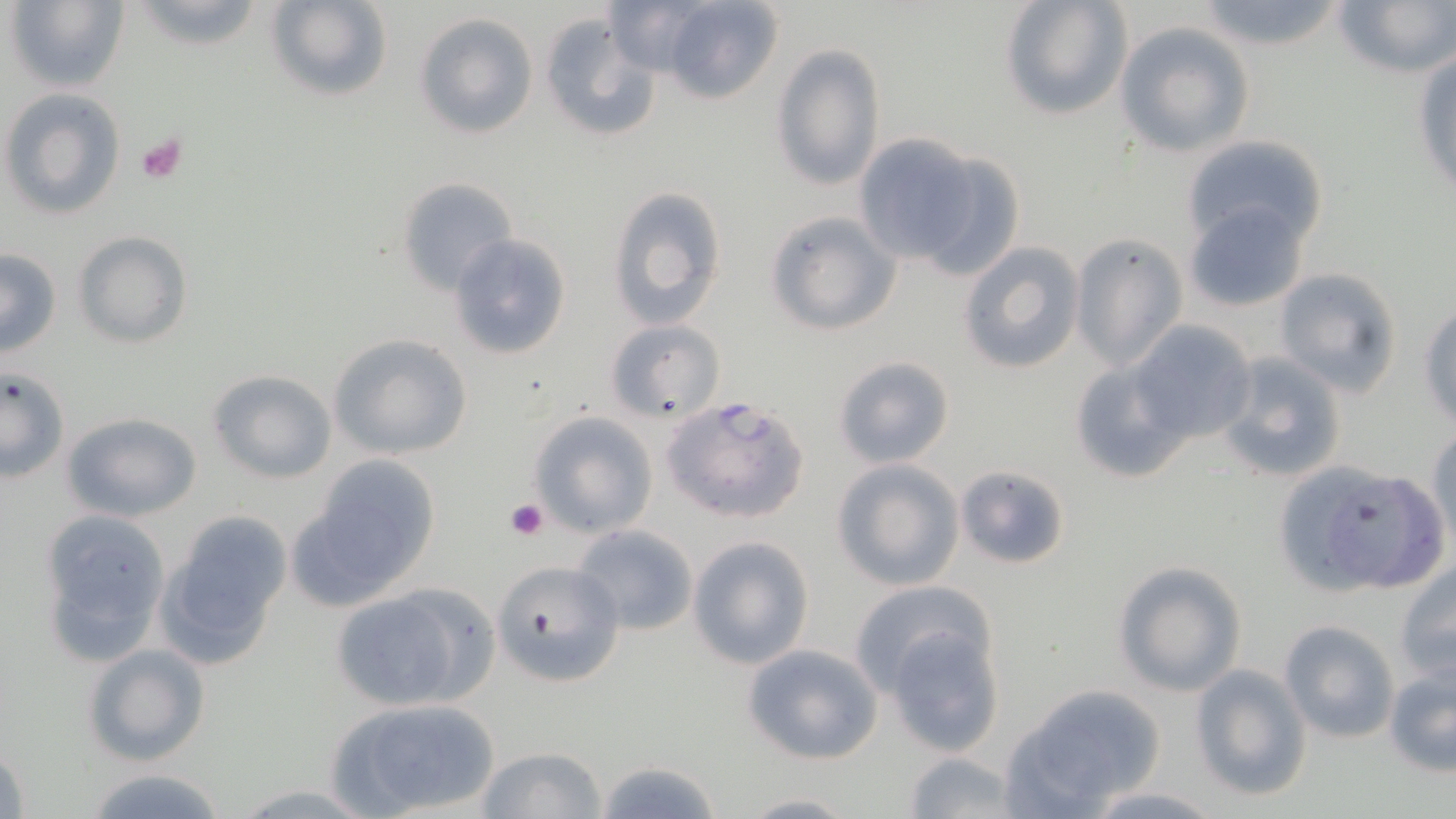
{
  "slide_level_diagnosis": "Plasmodium falciparum",
  "uninfected_red_blood_cell_locations": "approximate bounding boxes as [x1, y1, x2, y2] in pixels: [7, 0, 130, 94], [123, 0, 271, 51], [264, 0, 393, 103], [601, 0, 720, 77], [656, 0, 783, 104], [999, 0, 1131, 120], [1333, 0, 1455, 79], [1190, 1, 1350, 53], [416, 12, 538, 138], [539, 14, 661, 143], [1115, 22, 1255, 160], [771, 42, 887, 191], [1411, 51, 1456, 200], [2, 89, 126, 219], [852, 131, 997, 270], [1181, 135, 1329, 253], [913, 150, 1028, 280], [398, 176, 519, 297], [607, 185, 727, 330], [1184, 199, 1313, 313], [764, 210, 900, 335], [73, 230, 192, 350], [448, 233, 574, 361], [1069, 234, 1188, 371], [957, 241, 1087, 375], [0, 249, 61, 358], [1273, 268, 1404, 397], [1419, 301, 1455, 428], [604, 320, 724, 424], [1129, 321, 1256, 445], [328, 333, 473, 460], [1214, 350, 1348, 484], [832, 354, 956, 468], [1066, 356, 1191, 485], [0, 367, 69, 483], [208, 369, 336, 484], [528, 411, 658, 537], [62, 413, 202, 522], [1428, 427, 1456, 548], [297, 457, 441, 601], [832, 459, 965, 590], [1283, 460, 1396, 593], [954, 465, 1071, 569], [1341, 477, 1449, 589], [38, 510, 173, 666], [157, 511, 292, 668], [571, 524, 701, 635], [688, 536, 815, 671], [491, 556, 628, 687], [1113, 561, 1246, 695], [1396, 561, 1456, 680], [849, 582, 993, 693], [330, 586, 488, 711], [1279, 620, 1397, 744], [885, 628, 1005, 756], [741, 642, 884, 764], [82, 643, 211, 767], [1384, 661, 1456, 779], [1191, 664, 1311, 800], [1004, 684, 1167, 814], [326, 695, 502, 816], [1, 742, 30, 819], [475, 747, 607, 819], [901, 753, 1024, 819], [593, 758, 722, 818], [80, 764, 233, 819], [226, 783, 382, 816], [1080, 786, 1226, 818], [736, 792, 857, 817]",
  "image_size": "1456×819 pixels",
  "field_of_view": "one of a larger specimen",
  "stain": "May-Grünwald-Giemsa",
  "platelet_locations": "approximate bounding boxes as [x1, y1, x2, y2] in pixels: [134, 132, 187, 184], [505, 496, 550, 542]",
  "modality": "optical microscopy",
  "plasmodium_falciparum_infected_red_blood_cell_locations": "approximate bounding boxes as [x1, y1, x2, y2] in pixels: [663, 394, 811, 523]",
  "preparation": "thin blood film",
  "magnification": "1000x"
}